Classify this cell by malaria status.
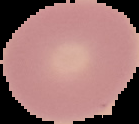
Uninfected.

image type = segmented cell region with the area outside set to black
image size = 139×124 pixels
preparation = thin blood film